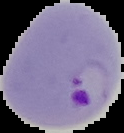
From a thin blood smear. Image is 124×133 pixels. Malaria status: parasitized. Segmented cell region on a black background.